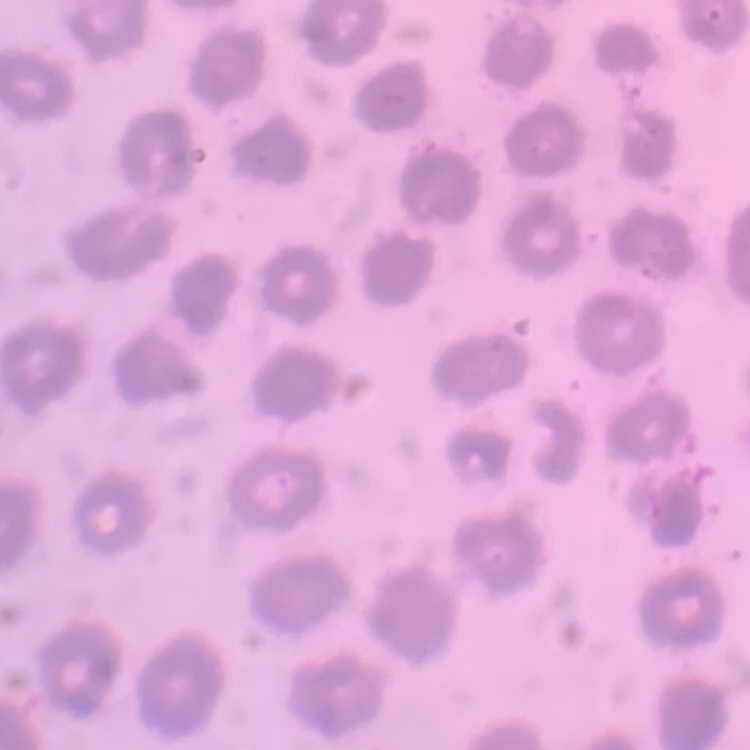
Summary:
  - Red blood cell morphology: no rouleaux formation
  - Stain: Field's or Giemsa
  - Preparation: thin blood smear
  - Image type: one tile cut from a larger photomicrograph